Assess this cell for malaria.
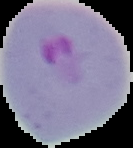
It is parasitized.

Summary:
  - Preparation: thin blood film
  - Image type: segmented cell region on a black background
  - Image size: 133×148 pixels